Assess for malaria.
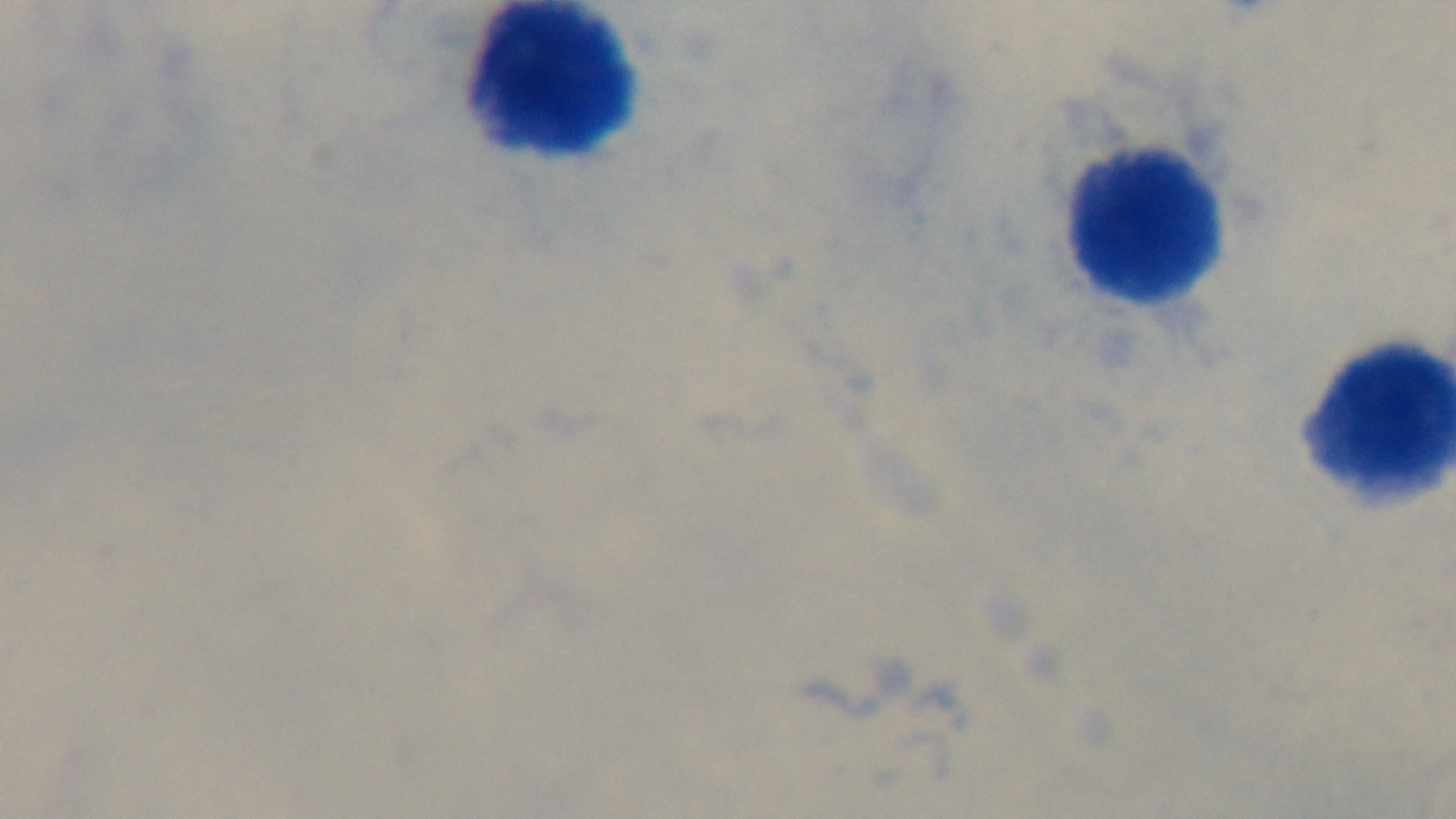
Uninfected.

field of view = one from the slide
stain = Giemsa
preparation = thick smear
capture = mounted 4K digital camera
objective = 100x oil immersion
modality = light microscopy